Point out every Plasmodium parasite.
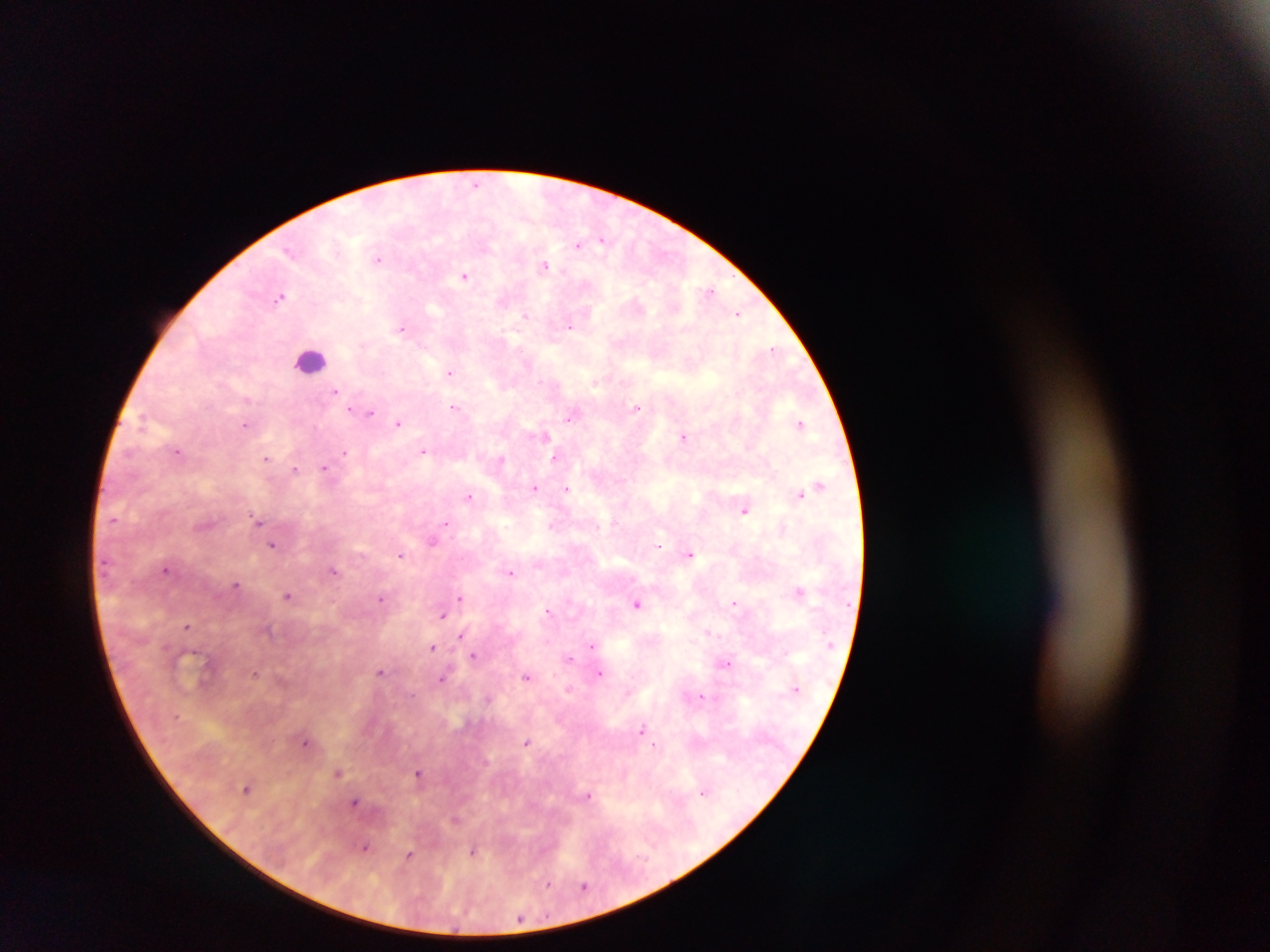
Approximate centers as x y in pixels.
Plasmodium parasites: 476 184; 603 240; 579 245; 290 251; 379 259; 546 266; 464 276; 711 290; 280 297; 525 314; 738 315; 570 327; 402 328; 773 348; 451 372; 335 391; 454 407; 637 409; 358 411; 372 413; 570 417; 398 423; 801 424; 246 425; 545 435; 684 437; 423 450; 177 451; 345 453; 267 458; 554 458; 294 469; 325 469; 820 485; 534 488; 567 489; 800 494; 469 496; 744 510; 113 520; 258 520; 445 522; 432 541; 272 545; 659 545; 690 554; 401 555; 166 570; 334 571; 511 573; 236 585; 800 591; 287 596; 381 598; 459 598; 735 603; 636 604; 548 610; 443 615; 187 626; 708 631; 462 635; 592 644; 432 647; 469 652; 474 656; 570 658; 727 663; 381 671; 254 673; 601 673; 526 676; 442 679; 701 695; 642 729; 305 743; 527 743; 656 745; 337 773; 419 773; 247 789; 704 792; 587 796; 356 802; 365 847; 472 852; 409 855; 548 885; 584 887; 520 918.

Summary:
  - Leukocyte locations: 310 360
  - Country: Ghana
  - Image size: 1270×952 pixels
  - Capture: mobile-phone photograph through a microscope
  - Preparation: thick blood film
  - Field of view: single